State which parasite is depicted.
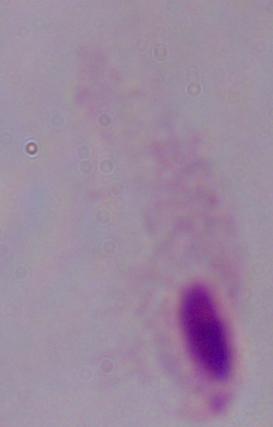

A trichomonad.

magnification: 1000x
modality: micrograph